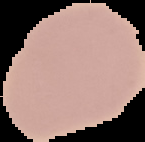
preparation = thin blood film
image type = segmented cell region on a black background
malaria status = uninfected
image size = 145×142 pixels